Identify the cell.
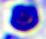

This is a leukocyte.

Summary:
  - Modality: micrograph
  - Magnification: 400x